Identify the parasite.
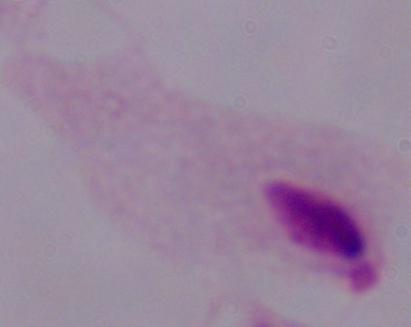
A trichomonad.

Captured at 1000x magnification. Photomicrograph.